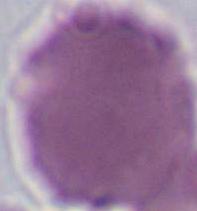
A red blood cell is shown. Photomicrograph. Captured at 1000x magnification.